Classify this cell by malaria status.
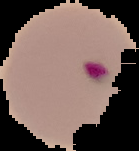

Parasitized.

Summary:
  - Image type: segmented cell region with the area outside set to black
  - Image size: 139×151 pixels
  - Preparation: thin blood smear